Look for parasitized red blood cells.
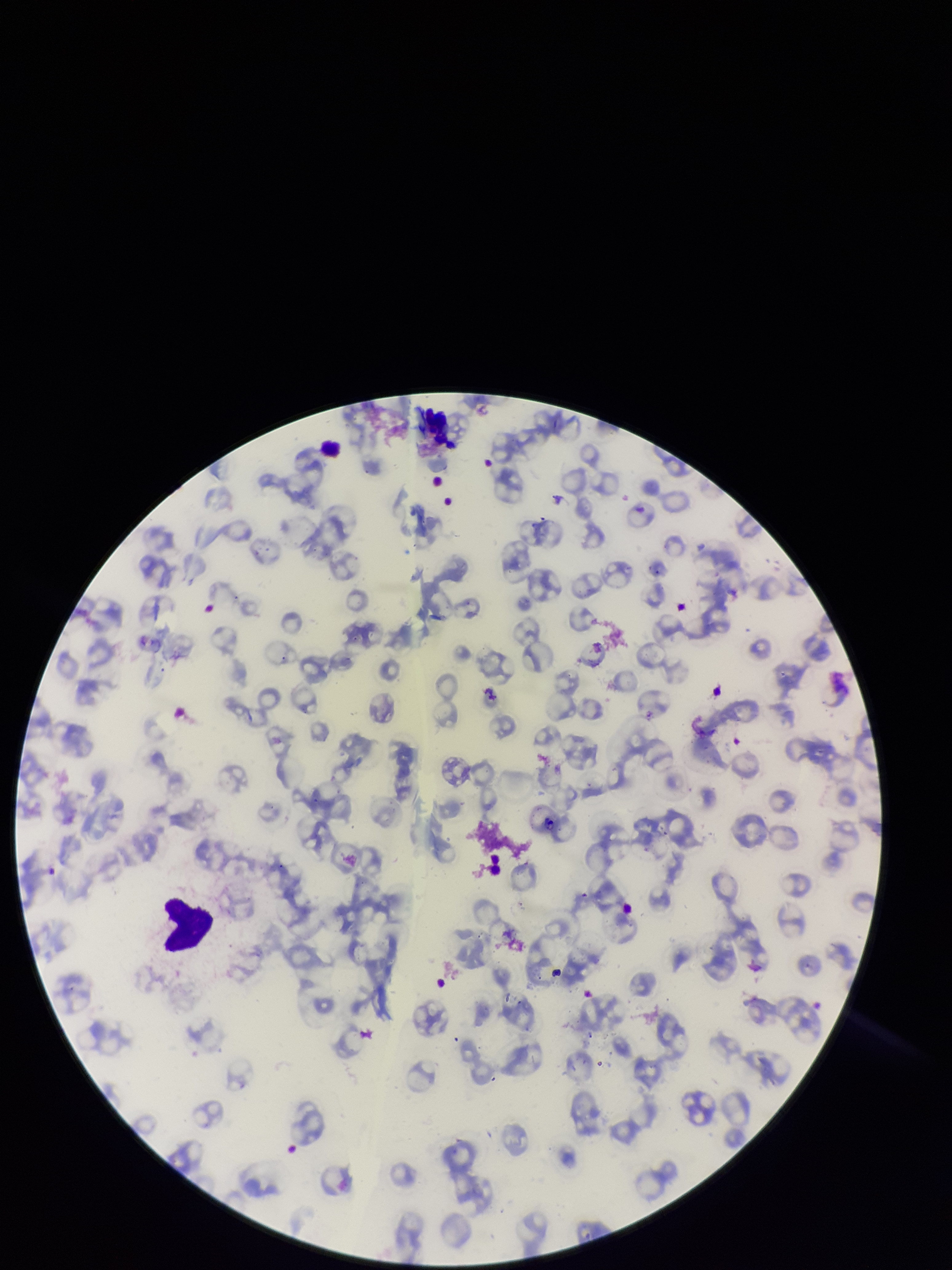

None identified.

Image is 952×1270 pixels. Photographed through the microscope eyepiece with a smartphone camera. Patient malaria status: infected. One field from this slide. Giemsa stain. Parasitized red blood cell count: 0. Species reported for this patient: Plasmodium falciparum. Preparation: thin. Red blood cell count: 100.